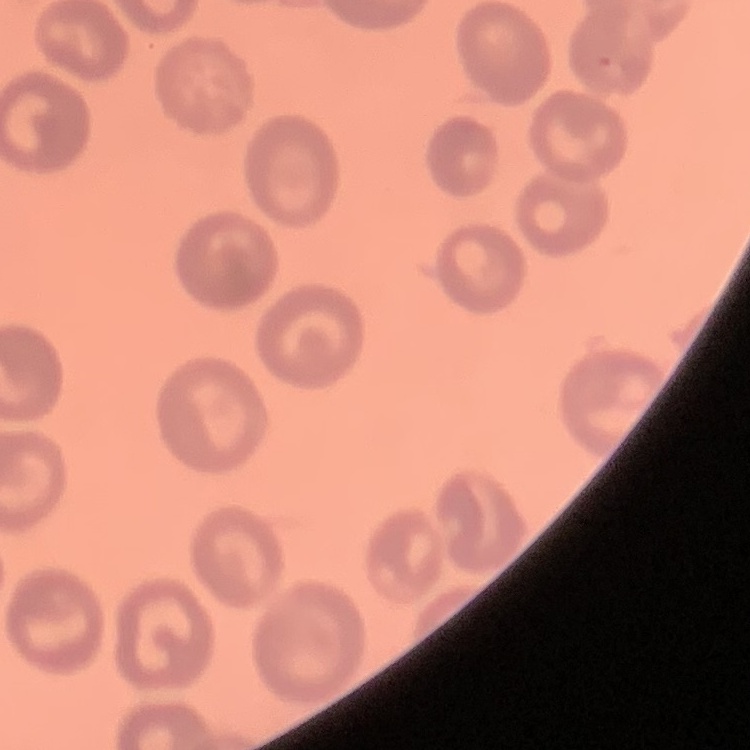

The red blood cells show no rouleaux formation. Field's or Giemsa stain. Square crop of a larger photomicrograph. Thin blood smear.